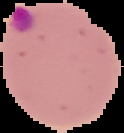

Malaria status: parasitized. From a thin blood smear. Segmented cell region on a black background. Image is 124×133 pixels.